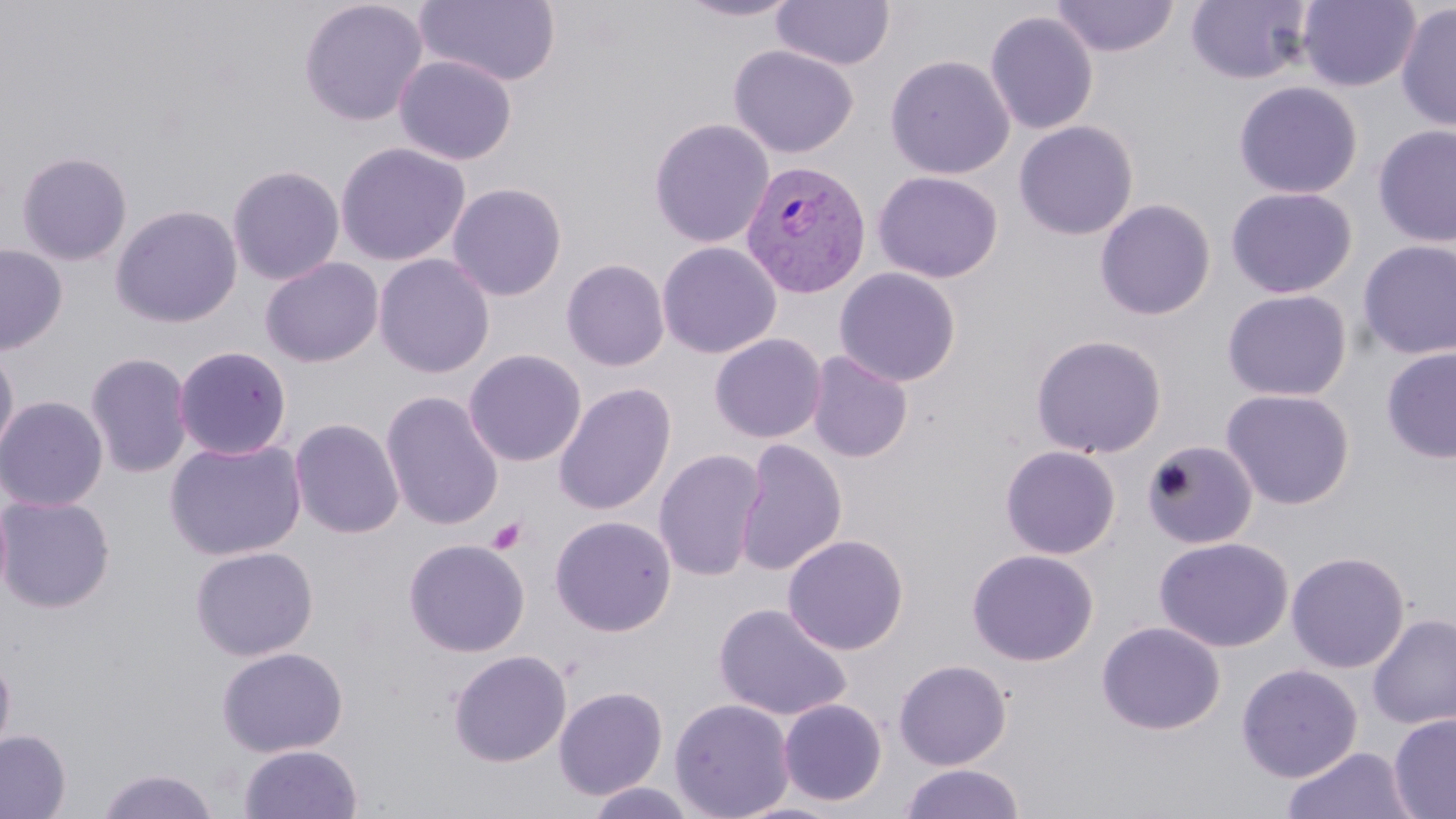

Plasmodium vivax-infected red blood cell locations = approximate bounding boxes as [x1, y1, x2, y2] in pixels: [741, 160, 873, 297]
slide-level diagnosis = Plasmodium vivax
magnification = 1000x
preparation = thin blood film
stain = May-Grünwald-Giemsa
modality = optical microscopy
uninfected red blood cell locations = approximate bounding boxes as [x1, y1, x2, y2] in pixels: [298, 0, 429, 127], [415, 0, 561, 87], [675, 0, 804, 22], [771, 0, 895, 70], [1050, 0, 1180, 57], [1297, 0, 1421, 92], [1185, 1, 1313, 85], [1395, 2, 1456, 132], [985, 11, 1099, 135], [728, 44, 858, 157], [885, 54, 1015, 179], [393, 55, 517, 165], [1233, 81, 1363, 198], [648, 118, 774, 249], [1013, 121, 1139, 240], [1373, 124, 1456, 247], [334, 142, 470, 266], [16, 151, 132, 266], [227, 164, 345, 286], [872, 170, 1003, 283], [447, 182, 567, 301], [1226, 186, 1358, 298], [1095, 198, 1216, 320], [109, 204, 243, 328], [1357, 240, 1456, 360], [657, 241, 781, 359], [0, 243, 68, 354], [373, 253, 495, 379], [260, 256, 384, 368], [561, 258, 671, 371], [834, 267, 962, 387], [1222, 289, 1353, 401], [709, 333, 827, 444], [1029, 333, 1167, 459], [0, 342, 20, 466], [173, 345, 293, 461], [1381, 347, 1456, 464], [463, 348, 587, 467], [85, 351, 193, 479], [806, 351, 913, 463], [554, 382, 676, 516], [1220, 387, 1356, 510], [380, 390, 504, 530], [0, 394, 108, 512], [289, 418, 404, 539], [164, 437, 307, 561], [735, 439, 847, 576], [1141, 440, 1258, 550], [1000, 445, 1121, 559], [653, 449, 766, 582], [0, 494, 116, 613], [549, 514, 677, 636], [782, 534, 909, 655], [403, 537, 530, 657], [1154, 537, 1293, 652], [189, 545, 319, 661], [965, 549, 1099, 666], [1286, 550, 1411, 673], [712, 602, 852, 722], [1367, 613, 1456, 730], [1096, 621, 1226, 735], [216, 645, 348, 757], [0, 649, 16, 765], [448, 649, 572, 767], [893, 659, 1012, 770], [1236, 663, 1363, 783], [553, 686, 669, 800], [669, 698, 795, 819], [778, 698, 888, 806], [1388, 713, 1456, 819], [0, 729, 70, 818], [238, 744, 363, 819], [1281, 746, 1418, 819], [899, 762, 1025, 819], [94, 767, 221, 819], [584, 781, 698, 819]
field of view = single
image size = 1456×819 pixels
platelet locations = approximate bounding boxes as [x1, y1, x2, y2] in pixels: [487, 517, 527, 555]